Report the malaria status of this cell.
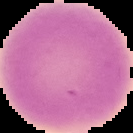

Uninfected.

Summary:
  - Preparation: thin blood film
  - Image size: 133×133 pixels
  - Image type: segmented cell region on a black background